Classify this cell by malaria status.
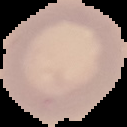
It is uninfected.

Summary:
  - Image size: 127×127 pixels
  - Preparation: thin blood film
  - Image type: segmented cell region with the area outside set to black